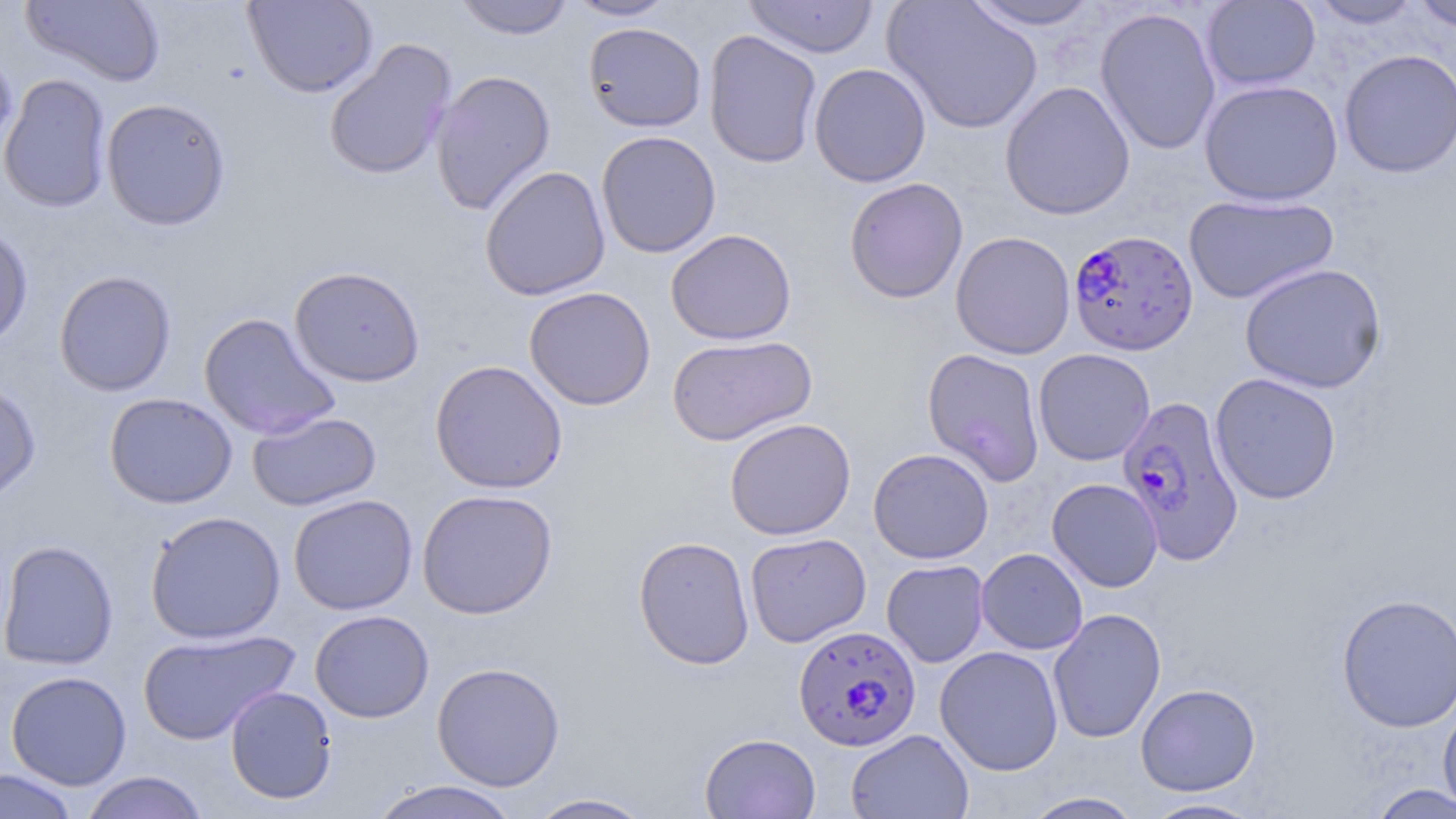
Approximate bounding boxes as (x1, y1, x2, y2) in pixels. Plasmodium falciparum-infected red blood cell locations: (1068, 229, 1199, 356), (1116, 395, 1245, 565), (792, 624, 921, 751). Uninfected red blood cell locations: (21, 0, 166, 87), (242, 0, 378, 98), (452, 0, 575, 40), (566, 0, 678, 21), (744, 0, 879, 59), (882, 0, 1043, 135), (1201, 0, 1321, 92), (1306, 0, 1424, 29), (1409, 0, 1456, 33), (964, 1, 1102, 31), (1096, 7, 1221, 156), (583, 22, 706, 133), (704, 29, 823, 169), (323, 38, 457, 182), (0, 48, 18, 161), (1339, 48, 1456, 178), (809, 63, 931, 187), (430, 68, 556, 215), (0, 73, 113, 213), (1199, 79, 1343, 206), (1000, 81, 1136, 220), (101, 98, 231, 231), (596, 130, 721, 258), (480, 165, 611, 301), (844, 177, 968, 304), (1184, 193, 1339, 305), (0, 224, 33, 352), (666, 229, 797, 345), (951, 231, 1076, 359), (1239, 263, 1387, 393), (288, 266, 425, 387), (54, 269, 176, 396), (524, 286, 656, 411), (199, 312, 341, 441), (667, 335, 817, 446), (922, 348, 1046, 486), (1033, 348, 1155, 466), (429, 359, 568, 494), (1209, 373, 1342, 504), (0, 381, 41, 503), (104, 392, 237, 509), (247, 410, 381, 512), (724, 418, 856, 541), (868, 448, 994, 563), (1047, 478, 1163, 592), (417, 489, 558, 619), (289, 494, 418, 615), (145, 510, 286, 643), (744, 532, 871, 647), (633, 536, 755, 670), (0, 540, 119, 670), (976, 548, 1088, 655), (882, 560, 989, 668), (1336, 593, 1456, 732), (1047, 608, 1166, 743), (309, 609, 434, 722), (137, 628, 301, 745), (934, 645, 1064, 776), (431, 661, 565, 791), (5, 671, 132, 789), (1135, 683, 1260, 796), (225, 686, 338, 805), (1438, 699, 1456, 816), (847, 729, 973, 818), (699, 733, 821, 818), (0, 768, 79, 819), (79, 771, 209, 819), (368, 781, 522, 819), (1366, 783, 1456, 818), (1020, 791, 1146, 818), (525, 793, 656, 818), (1142, 797, 1265, 818). Slide-level diagnosis: Plasmodium falciparum. Thin blood smear. 1000x magnification. Light microscopy. May-Grünwald-Giemsa-stained preparation. Single field of view. Image is 1456×819 pixels.